Assess the morphology of the erythrocytes.
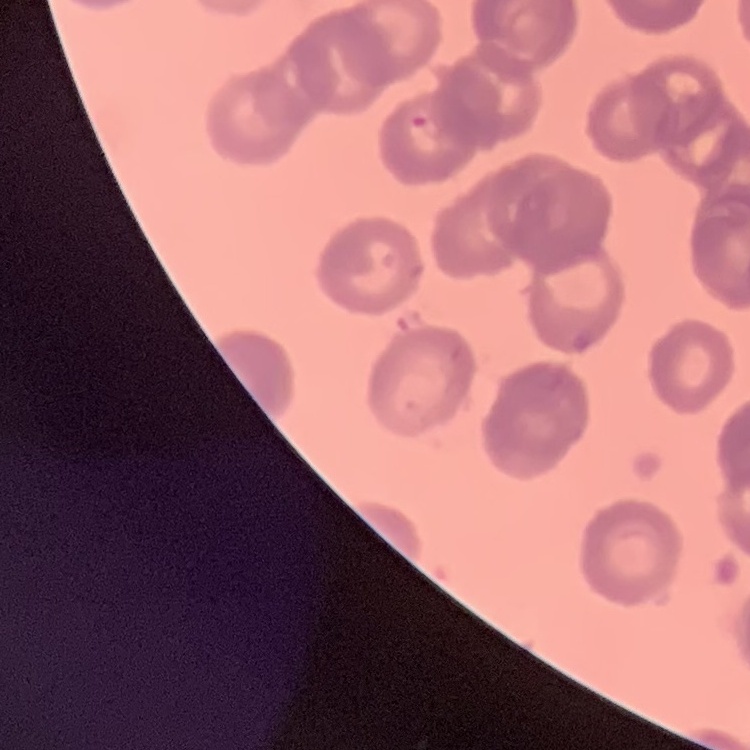

Rouleaux formation.

image type = square crop of a larger photomicrograph
stain = Field's or Giemsa
preparation = thin blood smear